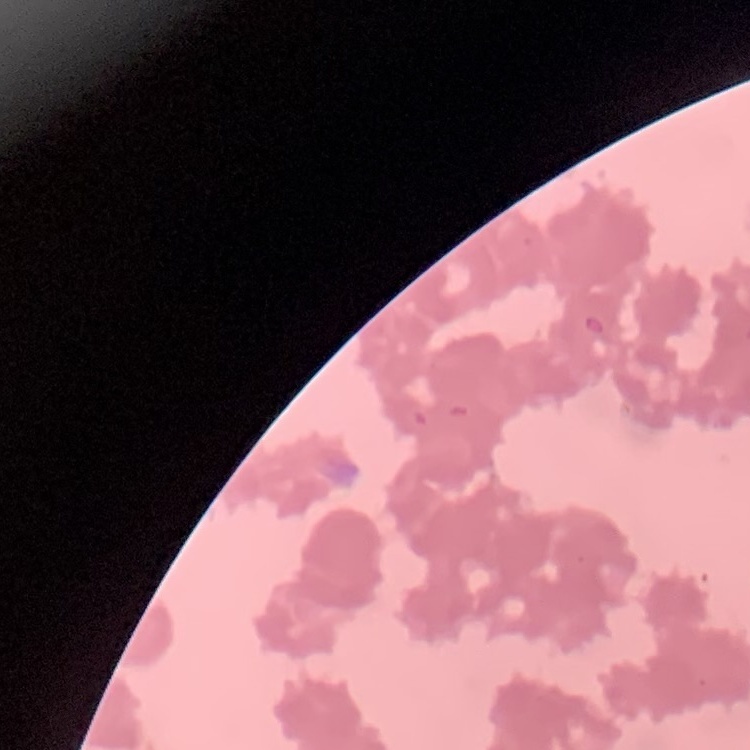
The erythrocytes exhibit rouleaux formation. One tile cut from a larger photomicrograph. Field's or Giemsa stain. Thin blood smear.